Assess the morphology of the red blood cells.
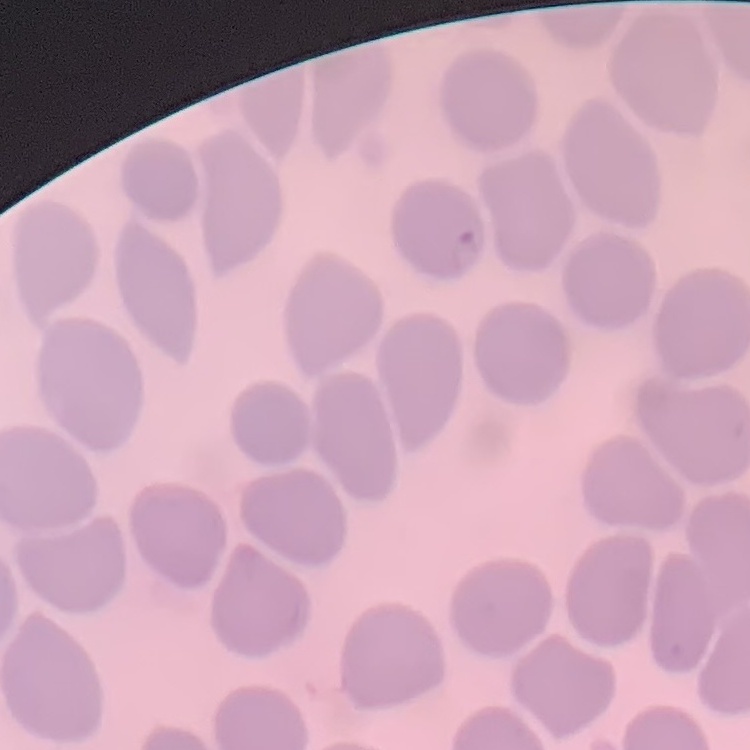
They show no rouleaux formation.

Summary:
  - Stain: Field's or Giemsa
  - Preparation: thin peripheral smear
  - Image type: one tile cut from a larger photomicrograph